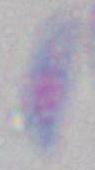

{
  "identification": "Toxoplasma gondii",
  "modality": "micrograph",
  "magnification": "1000x"
}